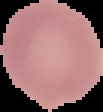

Summary:
  - Preparation: thin blood film
  - Image size: 103×112 pixels
  - Malaria status: uninfected
  - Image type: segmented cell region on a black background